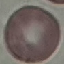 Result: no malaria parasites seen. Acquired by smartphone through the microscope eyepiece. Automatically extracted cell patch, resized to 64 × 64 pixels. Giemsa stain. Thin blood film.